Identify the cell.
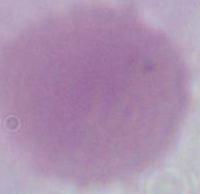

This is an erythrocyte.

1000x magnification. Micrograph.